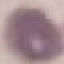
malaria status = uninfected
image type = cell patch, automatically extracted from a larger field of view and resized to 64 × 64 pixels
capture = smartphone through the microscope eyepiece
stain = Giemsa
preparation = thin blood smear